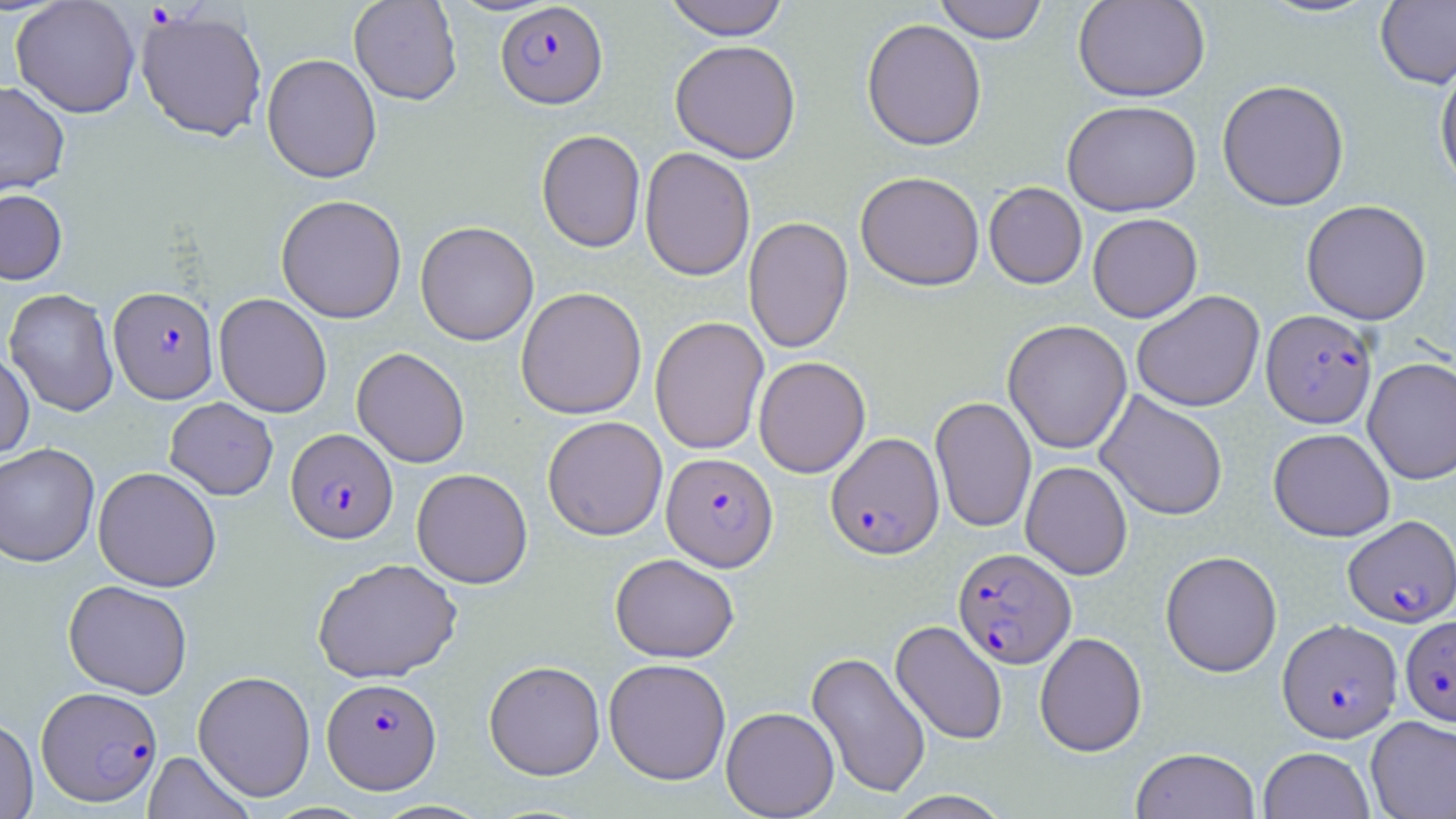

slide-level diagnosis = Plasmodium falciparum
modality = light microscopy
field of view = one of a larger specimen
Plasmodium falciparum-infected red blood cell locations = approximate bounding boxes as [x1, y1, x2, y2] in pixels: [496, 2, 608, 108], [108, 286, 219, 403], [1261, 309, 1377, 428], [285, 428, 398, 544], [826, 431, 944, 559], [661, 452, 778, 571], [1343, 514, 1456, 627], [952, 547, 1076, 668], [1400, 615, 1456, 725], [1278, 618, 1402, 742], [322, 677, 441, 793], [36, 686, 163, 807]
magnification = 1000x
image size = 1456×819 pixels
preparation = thin blood film
stain = May-Grünwald-Giemsa
uninfected red blood cell locations = approximate bounding boxes as [x1, y1, x2, y2] in pixels: [11, 0, 141, 118], [349, 0, 462, 105], [663, 0, 790, 39], [933, 0, 1049, 44], [1073, 0, 1210, 102], [1375, 0, 1456, 89], [135, 9, 268, 143], [861, 18, 987, 151], [670, 40, 801, 163], [261, 53, 382, 183], [1435, 59, 1456, 192], [1217, 79, 1349, 211], [0, 81, 70, 198], [1062, 100, 1202, 216], [536, 129, 646, 252], [640, 147, 755, 282], [855, 171, 985, 290], [984, 182, 1087, 289], [0, 188, 68, 284], [276, 194, 407, 323], [1301, 200, 1432, 325], [1087, 213, 1202, 323], [743, 216, 854, 354], [415, 221, 539, 346], [516, 287, 647, 419], [4, 288, 119, 416], [1131, 290, 1265, 412], [214, 293, 332, 417], [649, 316, 769, 455], [1003, 320, 1132, 454], [351, 347, 469, 468], [0, 350, 35, 460], [753, 356, 870, 478], [1363, 357, 1456, 485], [1095, 390, 1229, 521], [930, 396, 1036, 533], [165, 397, 278, 500], [542, 416, 668, 540], [1268, 427, 1395, 541], [0, 443, 100, 567], [1021, 461, 1133, 580], [93, 466, 222, 592], [411, 468, 533, 588], [1160, 550, 1282, 677], [610, 553, 739, 662], [312, 557, 462, 683], [63, 580, 193, 699], [890, 620, 1007, 745], [1034, 631, 1147, 756], [806, 651, 932, 799], [603, 658, 731, 785], [484, 660, 605, 780], [192, 669, 316, 802], [721, 706, 839, 817], [1365, 715, 1456, 819], [0, 716, 38, 818], [174, 728, 296, 815], [1130, 746, 1260, 819], [1259, 746, 1374, 819], [143, 751, 255, 819], [887, 790, 1012, 818]